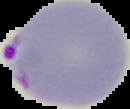
Summary:
  - Preparation: thin blood film
  - Image size: 130×109 pixels
  - Image type: segmented cell region with the area outside set to black
  - Malaria status: parasitized